Report the malaria status of this cell.
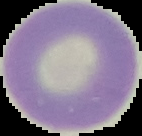

Uninfected.

{
  "preparation": "thin blood smear",
  "image_type": "cell region segmented out of the field of view; surrounding area masked to black",
  "image_size": "142×136 pixels"
}